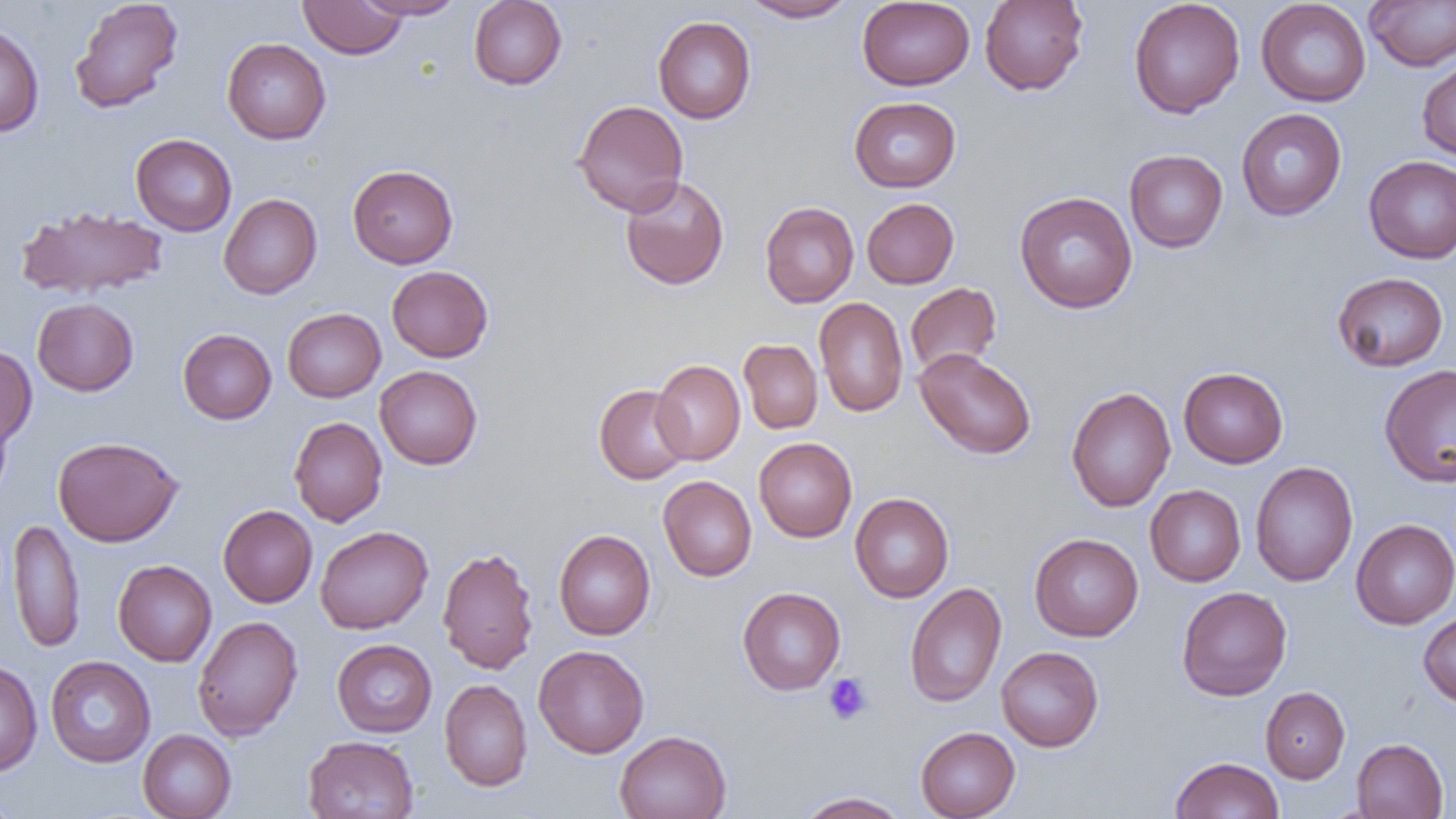

Approximate bounding boxes as [x1, y1, x2, y2] in pixels. Uninfected red blood cell locations: [69, 0, 184, 114], [354, 0, 465, 20], [468, 0, 567, 90], [740, 0, 858, 22], [979, 0, 1088, 96], [1128, 0, 1245, 118], [1256, 0, 1371, 107], [1364, 0, 1456, 71], [299, 1, 408, 59], [857, 1, 975, 90], [653, 16, 756, 124], [0, 21, 45, 137], [222, 38, 331, 144], [1417, 56, 1456, 163], [849, 96, 961, 192], [573, 99, 689, 216], [1236, 108, 1347, 221], [130, 133, 237, 236], [1124, 149, 1228, 253], [1364, 155, 1456, 264], [347, 164, 458, 268], [619, 175, 730, 291], [1015, 191, 1137, 314], [219, 193, 322, 299], [862, 197, 959, 289], [759, 202, 859, 308], [16, 205, 168, 300], [386, 265, 493, 362], [1332, 272, 1449, 372], [905, 282, 1002, 377], [814, 297, 908, 417], [32, 298, 139, 396], [282, 308, 386, 402], [177, 329, 277, 424], [738, 339, 823, 434], [0, 344, 37, 449], [914, 348, 1036, 459], [651, 359, 745, 465], [374, 365, 483, 470], [1379, 365, 1456, 486], [1178, 367, 1288, 468], [594, 384, 693, 484], [1066, 387, 1176, 512], [0, 407, 13, 507], [289, 416, 387, 527], [53, 436, 183, 547], [754, 437, 857, 542], [1250, 462, 1358, 586], [658, 475, 757, 581], [1145, 485, 1246, 586], [850, 493, 954, 602], [218, 504, 318, 607], [9, 517, 86, 653], [1351, 519, 1456, 629], [315, 526, 433, 634], [554, 529, 656, 640], [1030, 533, 1143, 641], [437, 546, 539, 675], [113, 559, 217, 666], [904, 582, 1007, 708], [1176, 586, 1292, 701], [737, 587, 846, 695], [1418, 610, 1456, 707], [192, 615, 303, 741], [331, 639, 437, 737], [533, 645, 649, 757], [996, 646, 1103, 751], [45, 656, 156, 767], [0, 661, 42, 776], [439, 679, 532, 791], [1261, 687, 1350, 783], [915, 726, 1020, 819], [138, 729, 237, 819], [615, 730, 732, 819], [303, 735, 419, 819], [1352, 738, 1448, 818], [1170, 756, 1284, 818], [0, 788, 21, 818], [797, 791, 911, 818]. Platelet locations: [823, 673, 873, 725]. Slide-level diagnosis: negative for blood parasites. Thin blood smear. Light microscopy. Image is 1456×819 pixels. One field of a larger specimen. Captured at 1000x magnification.